Classify this cell by malaria status.
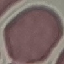

It is uninfected.

Cell patch, automatically extracted from a larger field of view and resized to 64 × 64 pixels. Acquired by smartphone through the microscope eyepiece. Giemsa-stained preparation. Thin smear of blood.